Identify the blood parasite species.
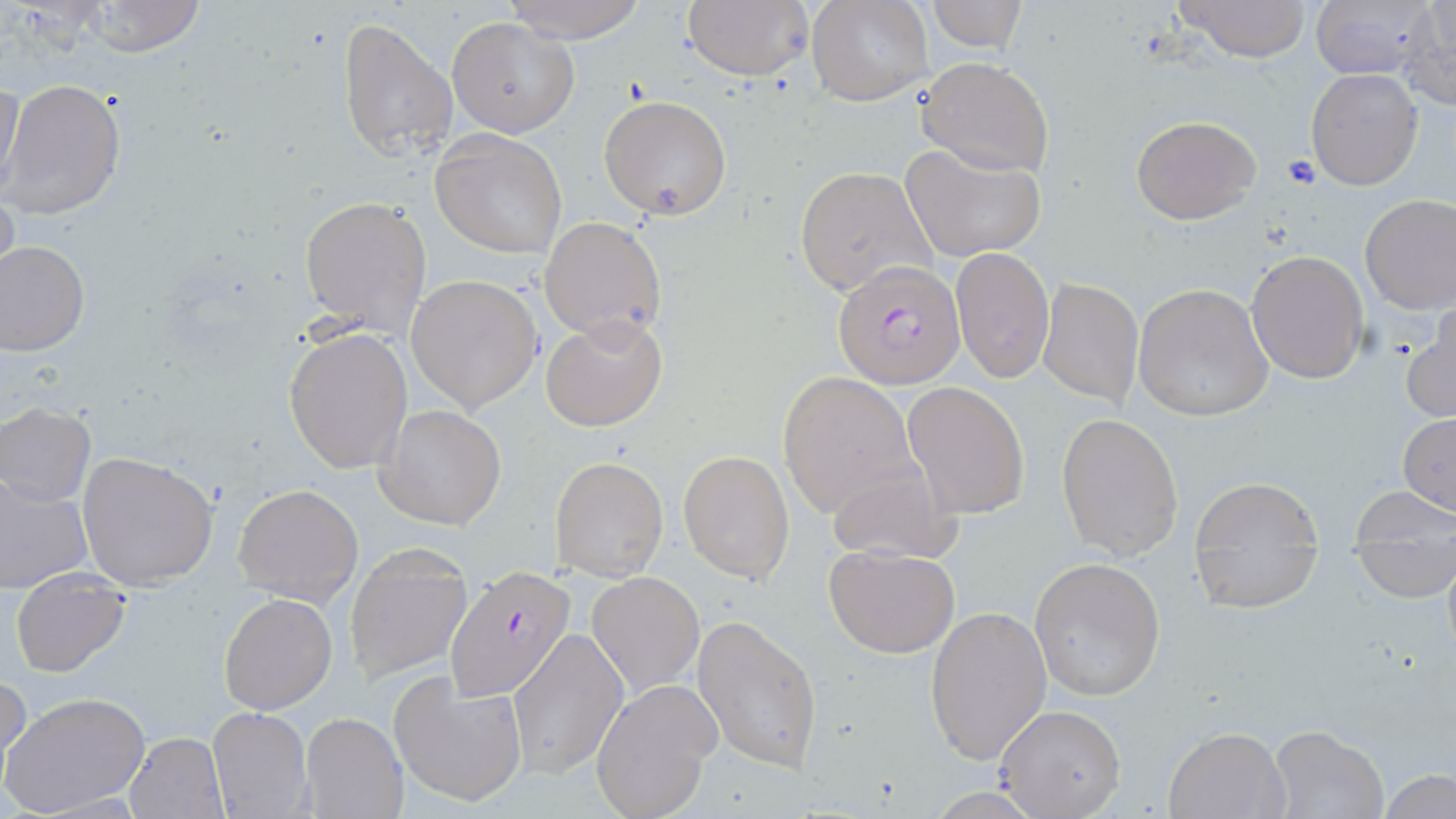
Plasmodium falciparum.

image_size: 1456×819 pixels
field_of_view: single
modality: optical microscopy
stain: May-Grünwald-Giemsa
plasmodium_falciparum_infected_red_blood_cell_locations: 'approximate bounding boxes as (x1, y1, x2, y2) in pixels: (834, 260, 964, 389), (443, 564, 576, 704)'
uninfected_red_blood_cell_locations: 'approximate bounding boxes as (x1, y1, x2, y2) in pixels: (680, 0, 813, 84), (807, 0, 931, 107), (1175, 0, 1313, 62), (1310, 0, 1437, 82), (1403, 0, 1456, 109), (76, 1, 209, 57), (499, 1, 651, 43), (927, 1, 1029, 53), (337, 15, 458, 165), (448, 16, 580, 138), (916, 57, 1053, 178), (1304, 67, 1425, 191), (1, 77, 25, 196), (2, 79, 127, 222), (599, 94, 732, 221), (1129, 113, 1261, 224), (430, 131, 567, 258), (901, 144, 1046, 262), (793, 164, 937, 299), (0, 183, 20, 301), (1359, 193, 1456, 314), (299, 195, 432, 336), (539, 216, 668, 342), (1, 241, 89, 356), (951, 247, 1054, 383), (1246, 249, 1369, 384), (407, 274, 544, 412), (1037, 276, 1145, 407), (1132, 282, 1275, 421), (1403, 303, 1456, 422), (541, 313, 668, 432), (284, 327, 415, 475), (776, 371, 918, 517), (902, 380, 1030, 519), (1, 402, 97, 506), (376, 403, 507, 530), (1056, 412, 1185, 562), (1398, 412, 1456, 516), (678, 448, 795, 583), (77, 451, 217, 589), (823, 455, 964, 566), (549, 456, 669, 582), (0, 472, 93, 595), (1186, 478, 1324, 614), (232, 482, 364, 605), (1353, 487, 1454, 544), (344, 541, 473, 685), (824, 545, 961, 658), (1352, 545, 1455, 601), (1028, 557, 1167, 701), (10, 570, 131, 677), (586, 571, 704, 697), (218, 593, 338, 715), (925, 604, 1051, 766), (693, 613, 824, 775), (507, 628, 628, 780), (0, 671, 31, 778), (389, 671, 529, 808), (590, 677, 717, 819), (2, 690, 151, 816), (996, 704, 1127, 817), (208, 707, 313, 818), (301, 711, 407, 819), (1163, 726, 1289, 818), (1267, 726, 1388, 819), (123, 732, 229, 818), (1380, 769, 1455, 818)'
preparation: thin blood film
magnification: 1000x